Locate every Plasmodium falciparum-infected red blood cell.
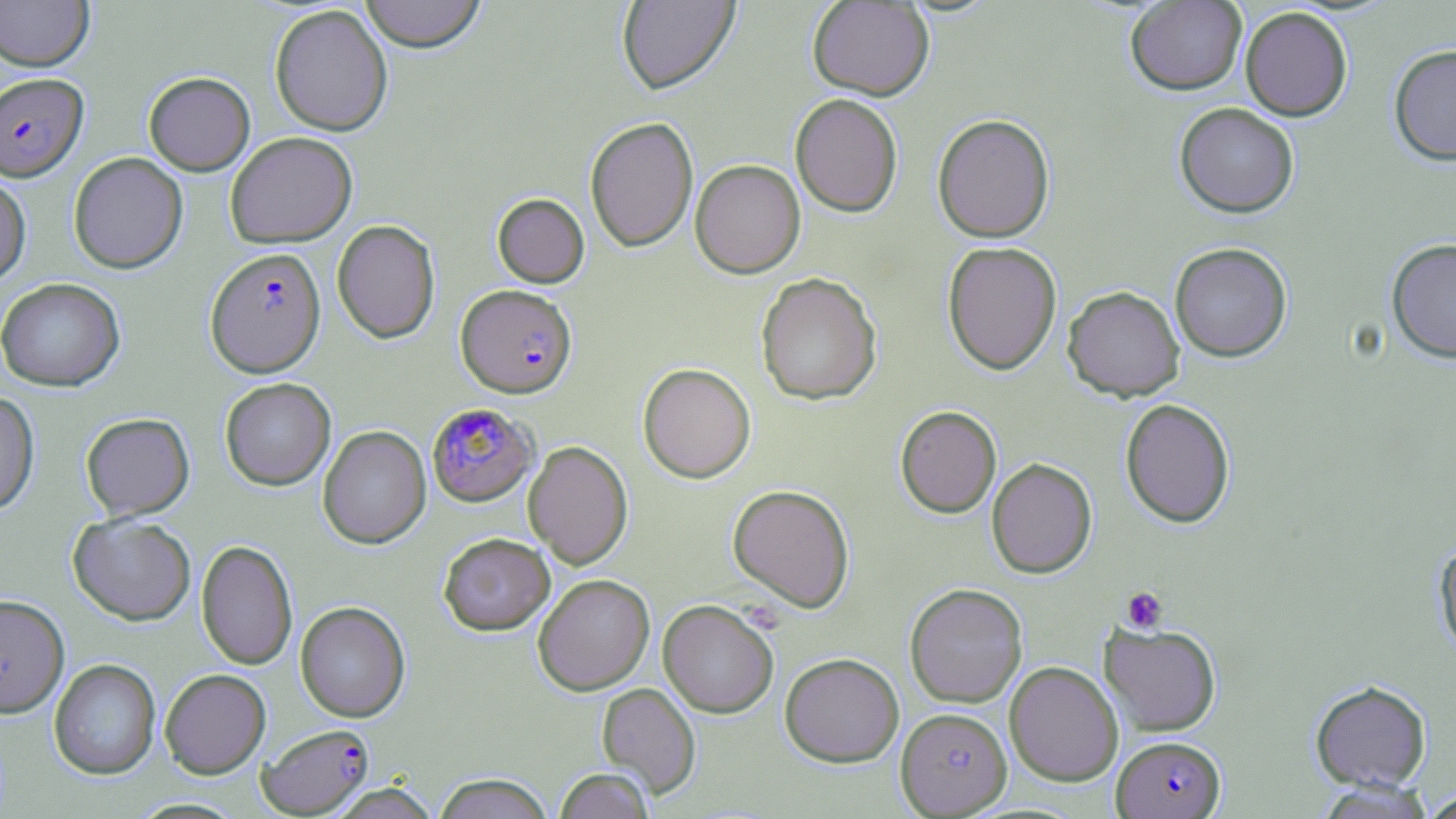

Approximate bounding boxes as named x1/y1/x2/y2 corners in pixels.
Plasmodium falciparum-infected red blood cells (subset): (x1=0, y1=72, x2=89, y2=181), (x1=205, y1=247, x2=326, y2=378), (x1=456, y1=284, x2=577, y2=397), (x1=427, y1=403, x2=537, y2=507), (x1=257, y1=724, x2=374, y2=817), (x1=1112, y1=736, x2=1225, y2=818).

{
  "slide_level_diagnosis": "Plasmodium falciparum",
  "field_of_view": "one of a larger specimen",
  "image_size": "1456×819 pixels",
  "uninfected_red_blood_cell_locations_subset": "approximate bounding boxes as named x1/y1/x2/y2 corners in pixels: (x1=0, y1=0, x2=94, y2=71), (x1=358, y1=0, x2=488, y2=53), (x1=616, y1=0, x2=741, y2=96), (x1=807, y1=1, x2=934, y2=100), (x1=1125, y1=1, x2=1247, y2=96), (x1=269, y1=4, x2=393, y2=136), (x1=1240, y1=7, x2=1353, y2=121), (x1=1388, y1=44, x2=1456, y2=166), (x1=143, y1=71, x2=255, y2=175), (x1=790, y1=94, x2=903, y2=217), (x1=1174, y1=102, x2=1299, y2=217), (x1=932, y1=113, x2=1056, y2=242), (x1=585, y1=116, x2=698, y2=252), (x1=225, y1=131, x2=357, y2=248), (x1=68, y1=152, x2=188, y2=273), (x1=690, y1=159, x2=806, y2=278), (x1=0, y1=173, x2=31, y2=287), (x1=492, y1=193, x2=589, y2=288), (x1=332, y1=219, x2=440, y2=344), (x1=1386, y1=237, x2=1456, y2=363), (x1=942, y1=241, x2=1062, y2=375), (x1=1169, y1=242, x2=1293, y2=362), (x1=755, y1=272, x2=882, y2=406), (x1=0, y1=278, x2=125, y2=391), (x1=1062, y1=285, x2=1184, y2=401), (x1=637, y1=362, x2=756, y2=483), (x1=220, y1=377, x2=336, y2=490), (x1=0, y1=390, x2=40, y2=516), (x1=1119, y1=398, x2=1236, y2=528), (x1=895, y1=405, x2=1001, y2=518), (x1=80, y1=412, x2=195, y2=520), (x1=317, y1=425, x2=431, y2=550), (x1=523, y1=441, x2=633, y2=570), (x1=986, y1=458, x2=1097, y2=578), (x1=727, y1=484, x2=855, y2=613), (x1=68, y1=513, x2=196, y2=625), (x1=439, y1=532, x2=555, y2=635), (x1=1432, y1=537, x2=1456, y2=660), (x1=196, y1=540, x2=298, y2=670), (x1=533, y1=574, x2=655, y2=696), (x1=904, y1=583, x2=1028, y2=708), (x1=658, y1=600, x2=779, y2=718), (x1=295, y1=601, x2=410, y2=723), (x1=1099, y1=621, x2=1222, y2=736), (x1=780, y1=653, x2=904, y2=767), (x1=49, y1=659, x2=161, y2=780), (x1=1004, y1=661, x2=1124, y2=786), (x1=160, y1=668, x2=271, y2=778), (x1=1309, y1=679, x2=1432, y2=792), (x1=596, y1=682, x2=701, y2=800), (x1=895, y1=707, x2=1012, y2=817), (x1=554, y1=767, x2=655, y2=818), (x1=433, y1=773, x2=554, y2=819), (x1=1313, y1=779, x2=1437, y2=818), (x1=326, y1=783, x2=441, y2=818), (x1=1420, y1=789, x2=1456, y2=819)",
  "stain": "May-Grünwald-Giemsa",
  "preparation": "thin blood smear",
  "magnification": "1000x",
  "platelet_locations": "approximate bounding boxes as named x1/y1/x2/y2 corners in pixels: (x1=1120, y1=586, x2=1169, y2=634)",
  "modality": "light microscopy"
}